Report the malaria status.
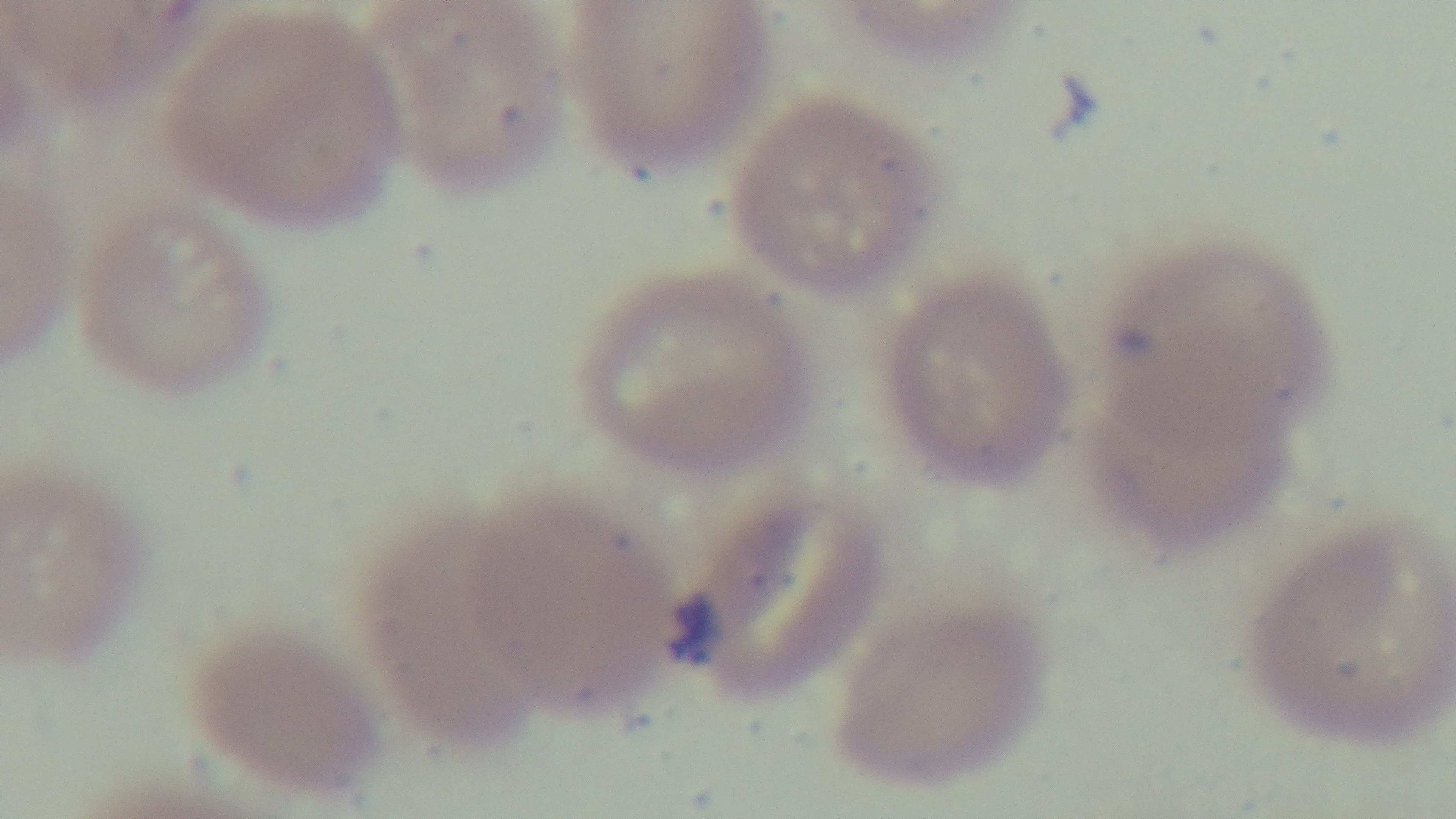

Positive.

Summary:
  - Capture: mounted 4K digital camera
  - Stain: Giemsa
  - Field of view: one from the slide
  - Modality: light microscopy
  - Preparation: thin smear
  - Objective: 100x oil immersion